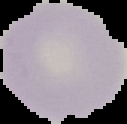

image_size: 127×124 pixels
result: no malaria parasites detected
preparation: thin blood film
image_type: segmented cell region with the area outside set to black